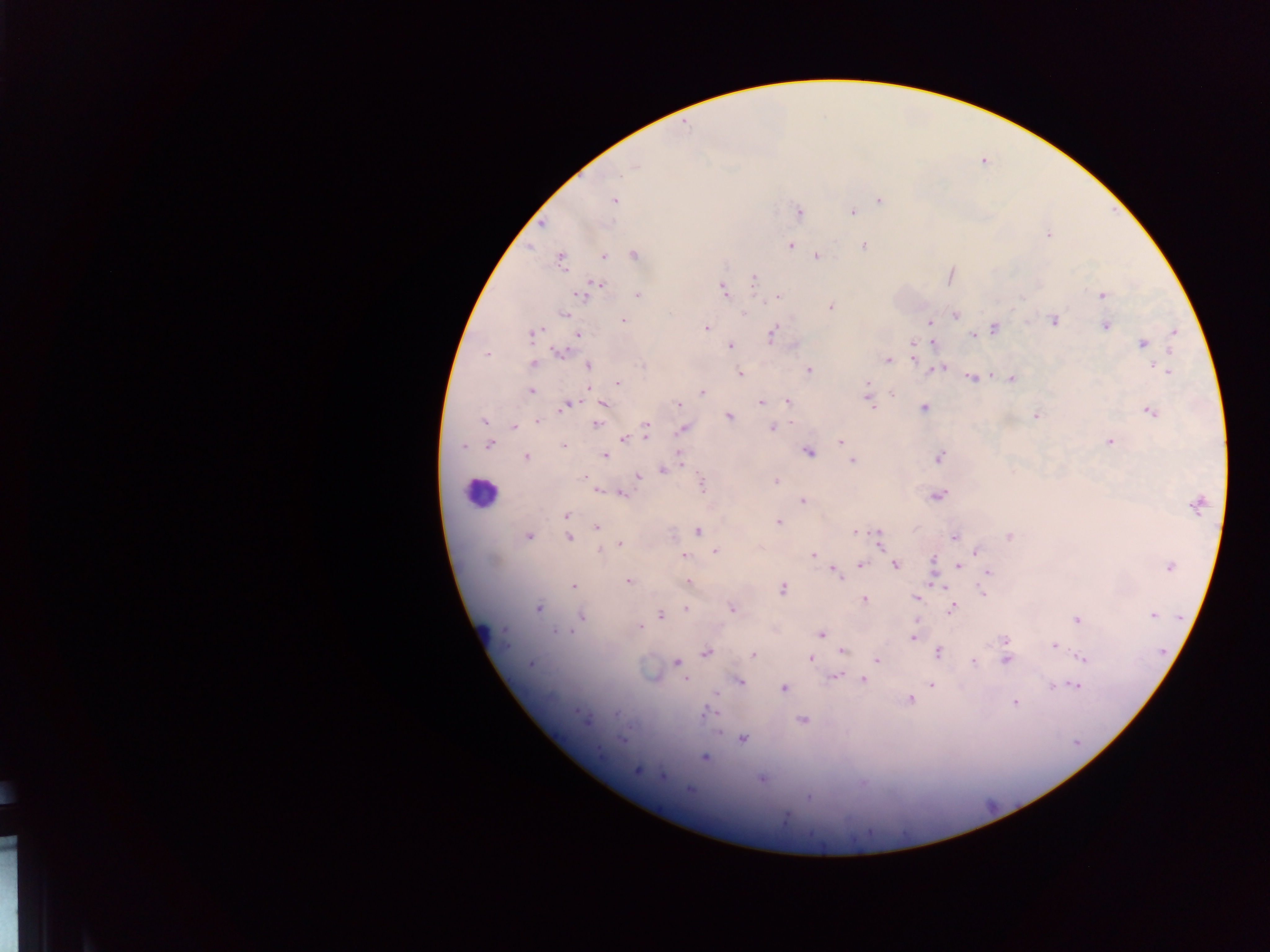
Approximate centers as x y in pixels. Malaria parasite locations: 685 128; 634 166; 879 199; 614 201; 798 210; 852 212; 1049 234; 790 244; 863 245; 634 253; 603 256; 817 257; 560 260; 754 279; 724 291; 584 294; 1101 295; 778 296; 639 298; 831 306; 745 314; 955 314; 624 321; 1052 321; 930 322; 1105 325; 993 327; 706 328; 538 330; 773 332; 1176 332; 531 333; 971 336; 529 338; 933 342; 911 343; 1142 344; 730 345; 558 352; 487 355; 887 359; 913 360; 533 363; 589 366; 640 367; 937 368; 944 368; 808 370; 1170 371; 739 372; 1011 377; 971 378; 867 384; 616 385; 531 391; 893 391; 702 392; 868 394; 604 402; 759 402; 787 403; 676 404; 870 405; 565 406; 925 409; 1150 411; 1036 415; 728 416; 483 422; 536 422; 594 424; 512 425; 772 426; 645 427; 681 429; 646 434; 645 439; 622 440; 1108 440; 838 441; 490 443; 563 447; 463 448; 678 452; 809 453; 527 456; 606 456; 940 456; 852 460; 683 465; 663 470; 582 477; 638 478; 775 480; 701 484; 597 489; 623 494; 938 496; 801 501; 1198 505; 565 515; 779 521; 597 528; 699 531; 529 534; 853 534; 569 536; 878 536; 955 536; 1009 536; 879 542; 621 543; 599 550; 715 551; 685 553; 976 553; 813 555; 933 559; 861 564; 895 566; 1169 566; 958 567; 834 572; 989 574; 838 578; 628 581; 687 581; 934 581; 573 586; 937 587; 783 588; 982 592; 864 598; 915 598; 539 608; 732 608; 686 609; 952 609; 583 613; 949 614; 1152 614; 660 615; 1075 619; 639 627; 820 635; 912 638; 1004 640; 1054 645; 843 651; 938 651; 706 653; 752 655; 811 658; 1083 659; 876 661; 1005 662; 531 663; 674 663; 974 664; 833 677; 862 678; 686 679; 741 683; 1052 685; 931 686; 1077 687; 783 689; 715 695; 909 700; 1015 703; 574 709; 705 712; 575 713; 615 716; 802 720; 587 722; 742 739; 621 740; 705 757; 637 771; 660 773; 761 780; 861 783; 690 790; 809 801; 787 818. One field of view. Sample from Ghana. Thick blood film. Image is 1270×952 pixels. Photographed through a microscope with a mobile-phone camera.